Assess this cell for malaria.
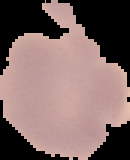
It is uninfected.

Summary:
  - Image size: 130×160 pixels
  - Image type: segmented cell region with the area outside set to black
  - Preparation: thin blood smear